Locate and identify every blood parasite.
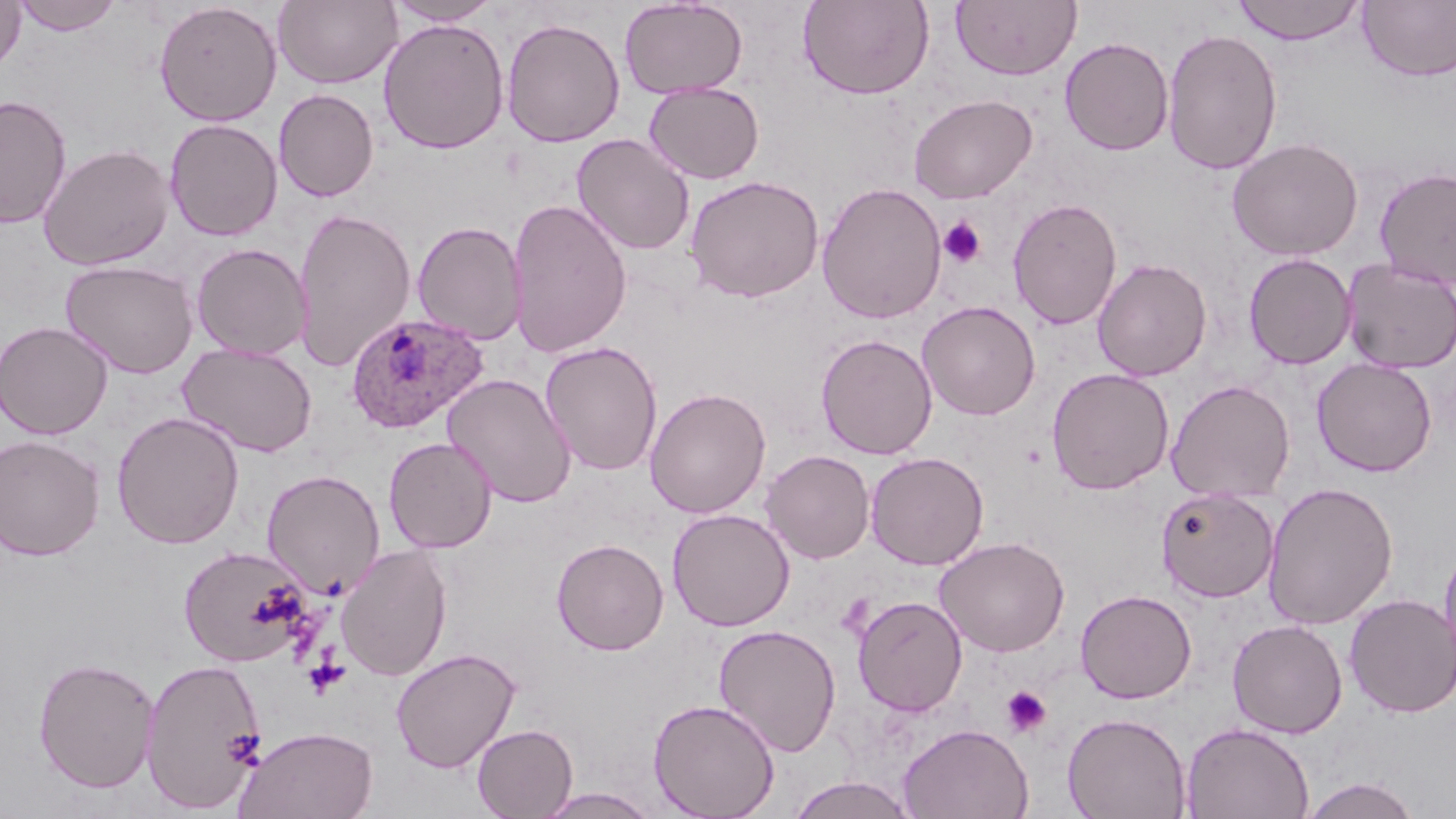

Approximate bounding boxes as (x1, y1, x2, y2) in pixels.
Plasmodium ovale-infected red blood cells: (345, 312, 488, 434).
No Plasmodium falciparum, Plasmodium malariae, Plasmodium vivax, Babesia divergens, or Trypanosoma brucei observed.

Uninfected red blood cell locations: (0, 0, 27, 74), (11, 0, 124, 35), (619, 0, 748, 99), (798, 0, 934, 100), (950, 0, 1081, 81), (1230, 0, 1366, 45), (154, 1, 282, 126), (274, 1, 402, 89), (386, 1, 501, 26), (1358, 1, 1456, 82), (501, 17, 625, 147), (377, 18, 511, 154), (1162, 28, 1283, 175), (1060, 37, 1174, 155), (644, 81, 765, 184), (274, 89, 379, 202), (908, 94, 1037, 204), (0, 95, 72, 228), (165, 118, 283, 241), (571, 133, 695, 255), (1226, 137, 1364, 261), (38, 143, 175, 270), (1374, 166, 1456, 291), (684, 174, 824, 302), (816, 182, 947, 324), (1008, 197, 1122, 330), (507, 198, 632, 357), (292, 207, 417, 373), (412, 221, 528, 344), (191, 242, 313, 360), (1243, 253, 1356, 369), (1092, 258, 1212, 382), (1340, 258, 1456, 373), (60, 259, 198, 379), (917, 300, 1040, 420), (0, 320, 113, 439), (815, 334, 938, 460), (540, 341, 663, 476), (178, 342, 318, 457), (1312, 357, 1438, 477), (1046, 367, 1174, 495), (442, 373, 577, 508), (1165, 379, 1295, 503), (644, 387, 771, 518), (111, 411, 245, 549), (0, 434, 105, 561), (383, 436, 498, 553), (760, 449, 875, 563), (865, 451, 989, 570), (261, 468, 384, 598), (1263, 481, 1398, 630), (1156, 486, 1279, 602), (667, 508, 795, 631), (934, 536, 1070, 657), (1438, 537, 1456, 679), (552, 538, 669, 655), (335, 544, 453, 681), (178, 545, 313, 667), (1075, 589, 1197, 704), (1344, 593, 1455, 718), (851, 594, 968, 717), (1227, 619, 1348, 738), (713, 624, 842, 756), (391, 647, 521, 773), (32, 656, 159, 793), (140, 657, 268, 812), (647, 698, 781, 818), (1062, 712, 1191, 819), (1181, 721, 1314, 819), (898, 723, 1034, 819), (472, 724, 578, 818), (234, 725, 379, 819), (785, 776, 920, 819), (1300, 777, 1422, 819), (534, 787, 660, 818). Platelet locations: (938, 216, 988, 269), (1001, 684, 1053, 738). Slide-level diagnosis: Plasmodium ovale. 1000x magnification. May-Grünwald-Giemsa stain. Single field of view. Light microscopy. Image is 1456×819 pixels. Thin blood smear.